Classify this cell by malaria status.
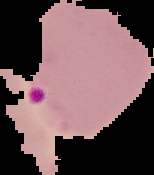

It is parasitized.

From a thin blood smear. Image is 154×175 pixels. Cell region segmented out of the field of view; the surrounding area is masked to black.